Assess this cell for malaria.
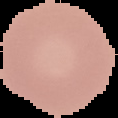
It is uninfected.

Summary:
  - Image size: 118×118 pixels
  - Image type: cell region segmented out of the field of view; surrounding area masked to black
  - Preparation: thin blood film